Assess this cell for malaria.
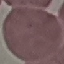

It is uninfected.

stain = Giemsa
capture = smartphone camera at the microscope eyepiece
image type = automatically extracted cell patch, resized to 64 × 64 pixels
preparation = thin smear